Assess this cell for malaria.
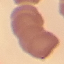
It is uninfected.

Summary:
  - Capture: smartphone camera at the microscope eyepiece
  - Stain: Giemsa
  - Image type: cell patch, automatically extracted from a larger field of view and resized to 64 × 64 pixels
  - Preparation: thin smear